Identify the blood parasite species.
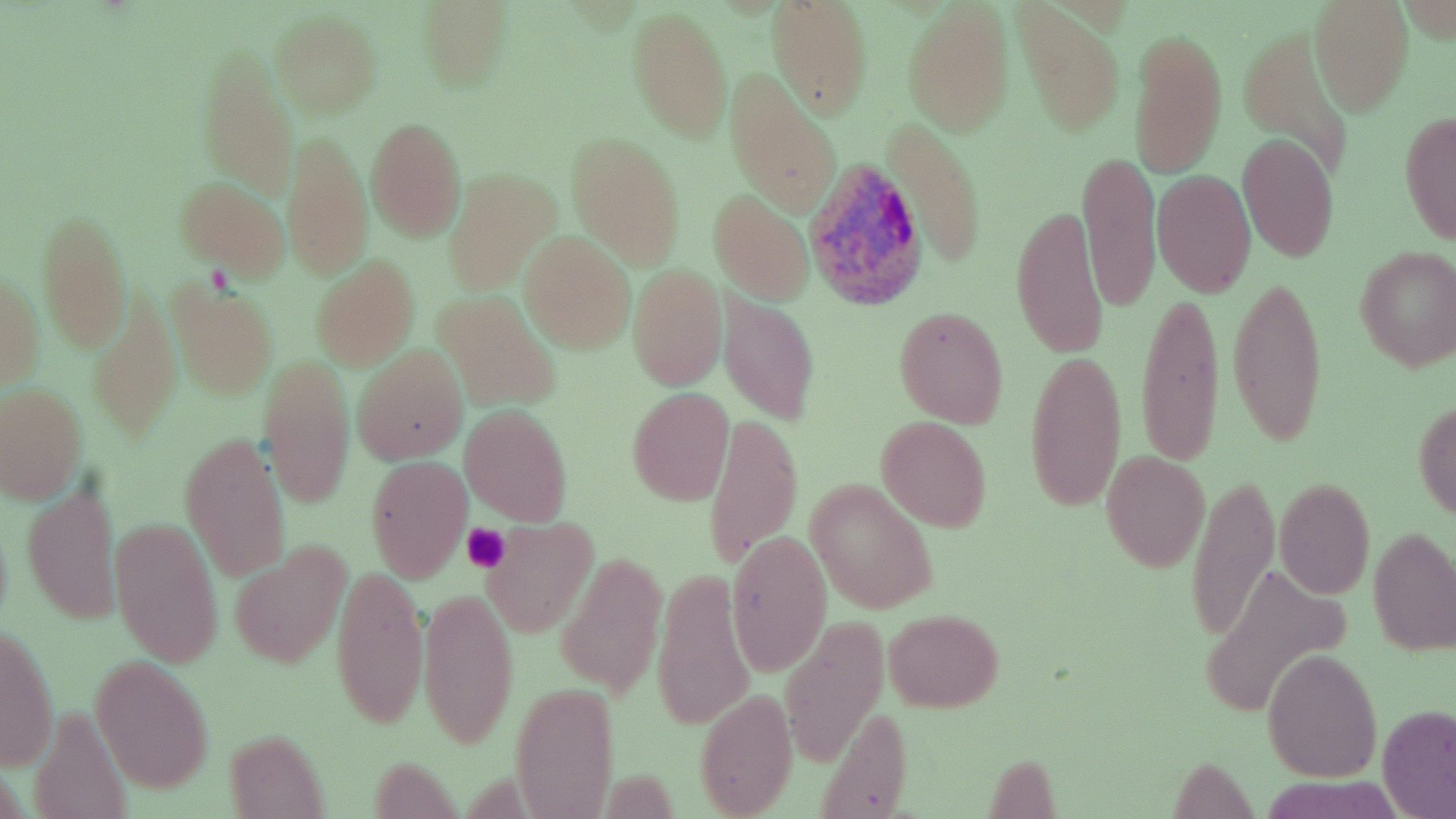

Plasmodium ovale.

Approximate bounding boxes as (x1,y1)-(x2,y2) corner pairs in pixels. Platelet locations: (460,524)-(511,572). Uninfected red blood cell locations: (416,1)-(513,92), (1309,1)-(1413,115), (765,2)-(873,119), (903,3)-(1013,137), (628,6)-(732,145), (1014,6)-(1124,137), (270,12)-(382,117), (1130,23)-(1227,181), (1236,26)-(1356,180), (197,52)-(298,198), (725,77)-(840,216), (1398,109)-(1456,247), (365,118)-(466,243), (888,119)-(988,271), (283,128)-(373,281), (566,132)-(685,269), (1238,133)-(1338,262), (1080,150)-(1160,313), (444,168)-(560,295), (1153,170)-(1256,296), (174,179)-(289,280), (710,189)-(813,305), (1011,201)-(1111,362), (37,207)-(130,354), (520,232)-(636,353), (1354,247)-(1456,371), (312,256)-(419,370), (0,264)-(43,392), (628,265)-(725,392), (1226,271)-(1330,453), (168,281)-(278,398), (88,290)-(181,441), (1137,290)-(1225,471), (436,292)-(560,410), (718,296)-(820,425), (892,306)-(1009,428), (352,345)-(467,464), (1024,349)-(1127,514), (261,352)-(356,511), (0,384)-(84,502), (627,388)-(734,507), (1412,399)-(1456,520), (460,405)-(573,526), (702,408)-(802,572), (875,416)-(992,531), (179,430)-(288,583), (1102,451)-(1208,571), (366,456)-(471,582), (1185,474)-(1277,646), (1275,479)-(1374,600), (805,480)-(939,614), (23,482)-(120,625), (111,518)-(222,668), (481,518)-(597,638), (1368,528)-(1456,655), (726,530)-(831,676), (230,544)-(350,670), (557,555)-(666,697), (1201,562)-(1353,718), (331,563)-(429,731), (651,567)-(755,734), (418,586)-(516,751), (886,609)-(1001,712), (780,617)-(885,763), (1,625)-(59,772), (1262,649)-(1382,780), (92,660)-(213,793), (510,684)-(619,819), (695,690)-(797,818), (29,701)-(135,819), (815,704)-(916,816), (1376,707)-(1455,818), (224,730)-(328,816), (366,758)-(462,815), (1167,759)-(1257,814). Plasmodium ovale-infected red blood cell locations: (801,156)-(924,309). Thin blood smear. Captured at 1000x magnification. Image is 1456×819 pixels. Optical microscopy. May-Grünwald-Giemsa-stained preparation. Single field of view.